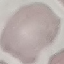 Result: no malaria parasites seen. Photographed with a smartphone camera at the microscope eyepiece. Giemsa-stained preparation. Cell patch, automatically extracted from a larger field of view and resized to 64 × 64 pixels. Thin smear of blood.